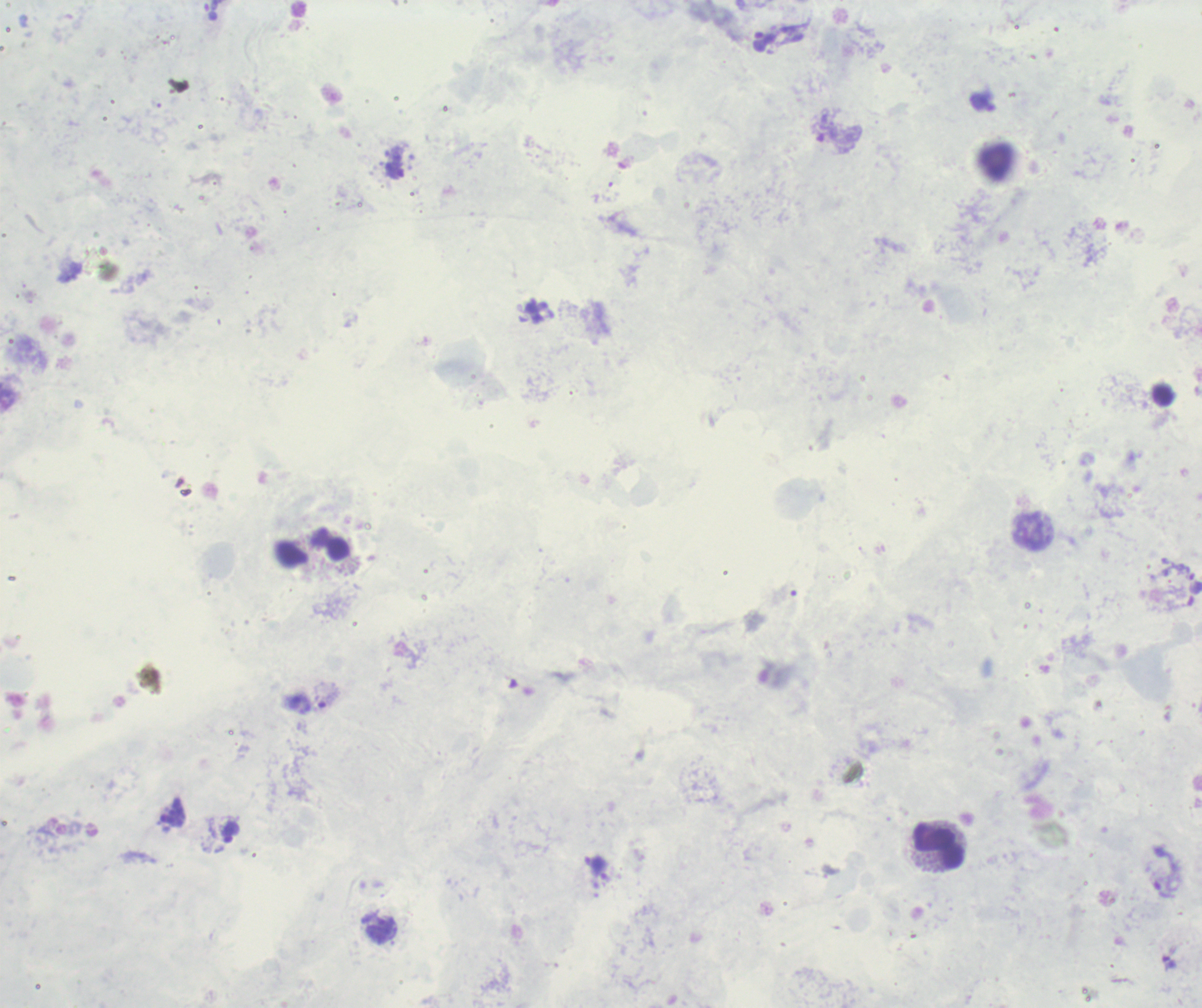
Approximate object centers, in pixels from the top-left corner.
Summary:
  - Trophozoite locations: (x=765, y=41), (x=326, y=698), (x=230, y=833), (x=1166, y=872), (x=1169, y=962)
  - Leukocyte locations: (x=995, y=162), (x=329, y=544), (x=939, y=846)
  - Field of view: one from this slide
  - Context: previously used in an actual diagnosis
  - Preparation: thick blood film
  - Magnification: 100x
  - Stain: Romanowsky
  - Background quality: poor
  - Result: malaria parasites identified
  - Image size: 1202×1008 pixels